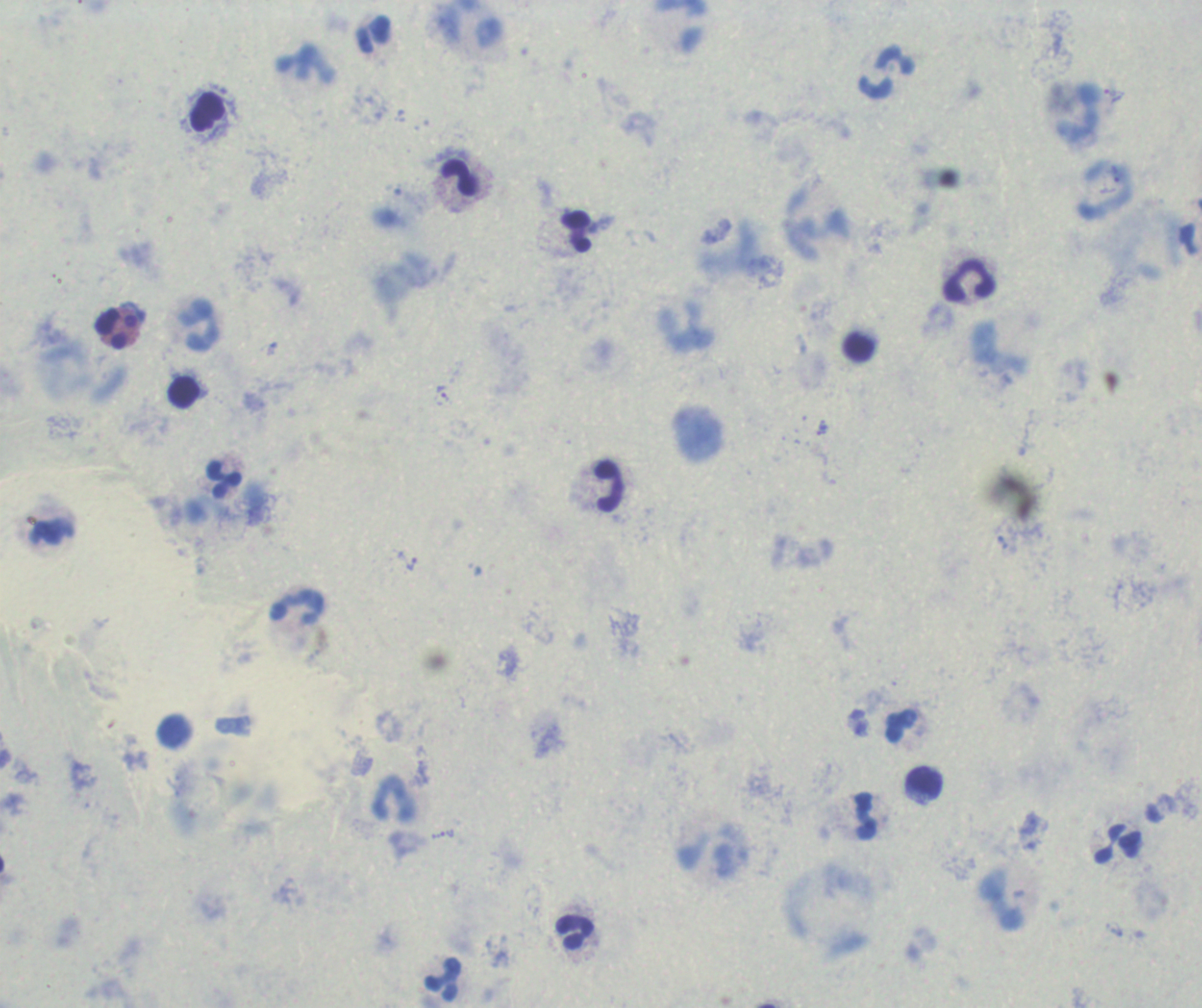
coordinate format = approximate centers as [x, y] in pixels
trophozoite locations = [1114, 95], [442, 396], [407, 561], [443, 834]
leukocyte locations = [372, 36], [305, 63], [886, 73], [206, 112], [459, 178], [1107, 191], [576, 232], [970, 280], [200, 327], [116, 329], [859, 348], [184, 391], [224, 479], [608, 486], [297, 605], [901, 726], [175, 730], [924, 782], [395, 799], [866, 816], [1118, 843], [576, 932], [444, 980]
image size = 1202×1008 pixels
preparation = thick smear of blood
field of view = one from this slide
stain = Romanowsky
magnification = 100x
result = malaria parasites detected
background quality = unsatisfactory
context = previously used in an actual diagnosis